Name the parasite shown.
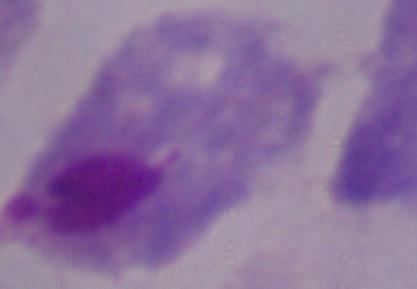

This is a trichomonad.

Summary:
  - Magnification: 1000x
  - Modality: photomicrograph